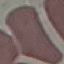
Summary:
  - Result: no malaria parasites seen
  - Stain: Giemsa
  - Image type: automatically extracted cell patch, resized to 64 × 64 pixels
  - Capture: smartphone through the microscope eyepiece
  - Preparation: thin smear